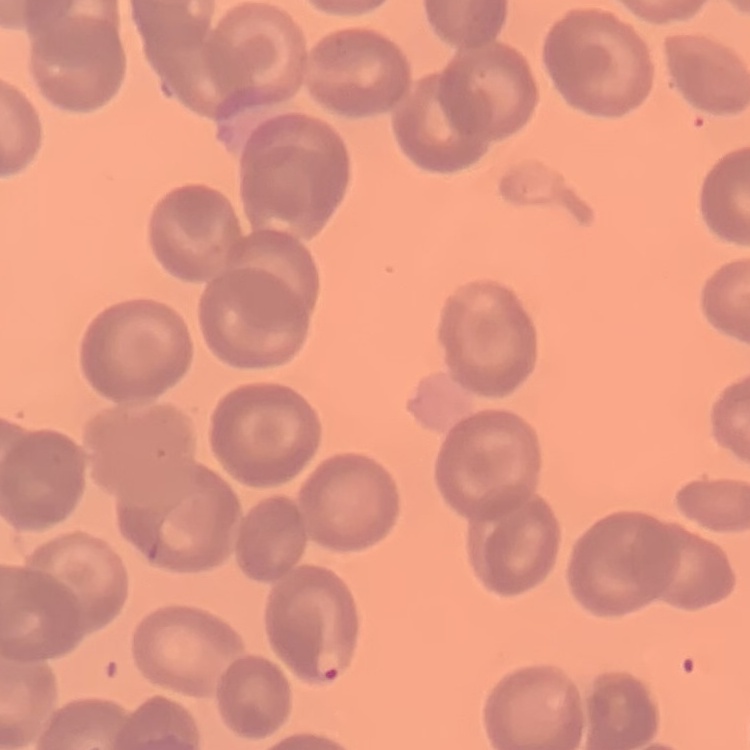

Summary:
  - Red blood cell morphology: no rouleaux formation
  - Preparation: thin blood smear
  - Image type: one tile cut from a larger photomicrograph
  - Stain: Field's or Giemsa